Outline each blood parasite and name the species.
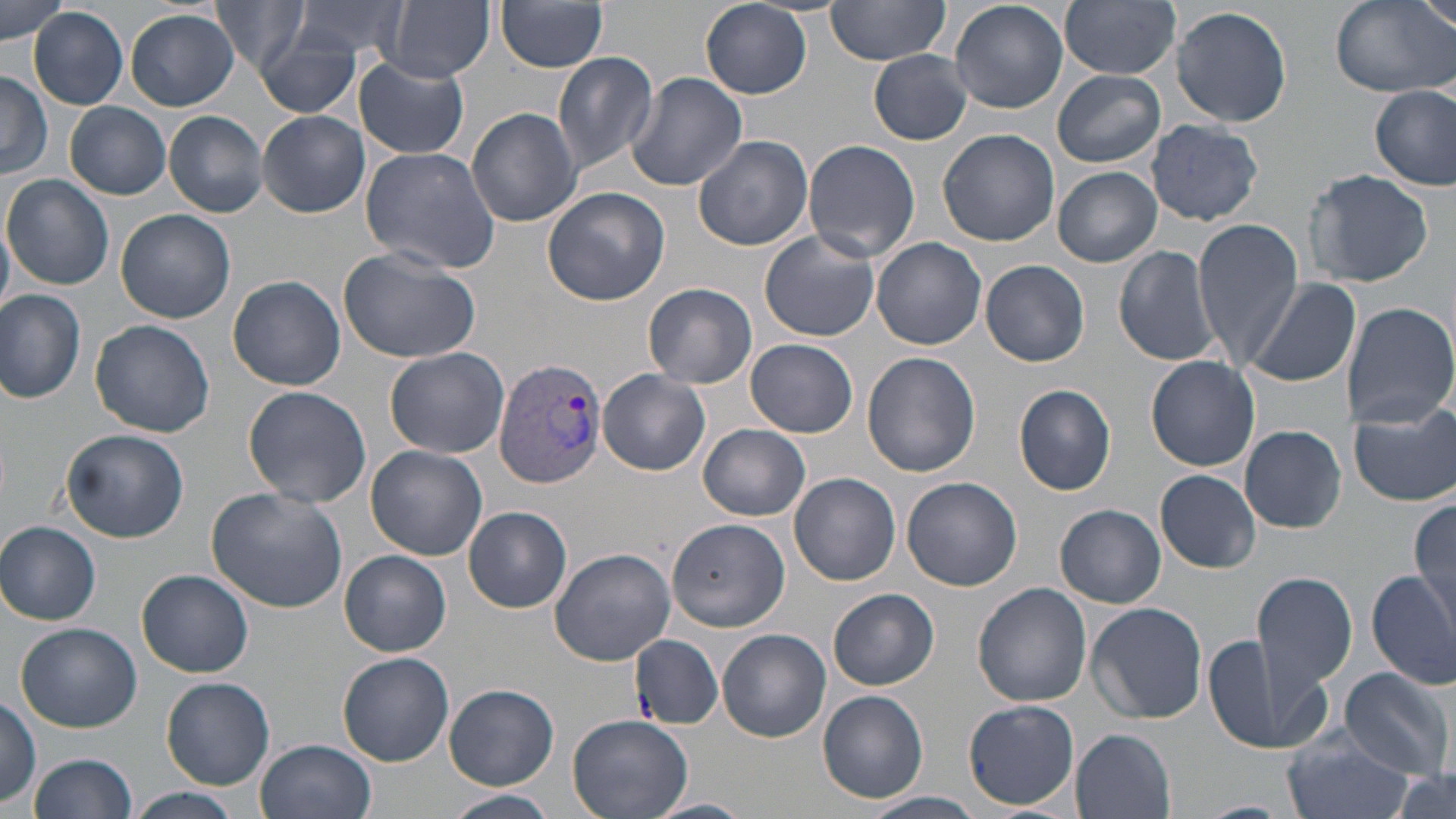
Approximate bounding boxes as (x1,y1)-(x2,y2) corner pairs in pixels.
Plasmodium vivax-infected red blood cells: (495,357)-(611,489).
No Plasmodium falciparum, Plasmodium ovale, Plasmodium malariae, Babesia divergens, or Trypanosoma brucei observed.

Summary:
  - Uninfected red blood cell locations: (0,0)-(70,44), (209,0)-(313,77), (291,0)-(411,62), (384,0)-(494,81), (824,0)-(952,64), (950,0)-(1070,112), (1061,0)-(1181,78), (1330,0)-(1454,98), (1420,0)-(1456,35), (495,1)-(609,72), (700,1)-(812,98), (1170,4)-(1294,129), (28,7)-(129,110), (126,9)-(238,110), (253,31)-(363,117), (870,50)-(974,145), (552,51)-(659,175), (354,55)-(470,160), (0,70)-(50,178), (1052,70)-(1165,167), (624,72)-(748,191), (1371,84)-(1455,191), (65,101)-(172,200), (466,106)-(581,227), (258,110)-(369,218), (164,111)-(269,217), (1147,119)-(1264,226), (938,129)-(1059,246), (693,134)-(814,251), (805,138)-(919,263), (359,146)-(503,275), (1052,165)-(1161,268), (1303,169)-(1433,287), (3,174)-(114,290), (542,186)-(671,306), (116,208)-(236,323), (1194,218)-(1303,370), (0,221)-(14,318), (759,230)-(880,342), (872,238)-(988,351), (1112,245)-(1222,367), (338,246)-(479,364), (980,258)-(1090,367), (227,276)-(346,390), (1246,278)-(1359,390), (643,282)-(757,389), (0,289)-(87,405), (1340,300)-(1456,429), (89,319)-(216,438), (746,339)-(858,438), (384,348)-(509,457), (862,352)-(980,477), (1145,356)-(1260,471), (599,370)-(710,476), (1013,383)-(1116,496), (242,385)-(371,508), (1349,400)-(1456,508), (698,423)-(811,522), (1240,426)-(1348,533), (61,428)-(188,543), (366,446)-(490,562), (1157,471)-(1261,574), (789,473)-(900,584), (901,475)-(1022,591), (206,485)-(351,613), (1412,498)-(1454,634), (1056,505)-(1166,608), (462,506)-(572,614), (667,518)-(790,632), (0,521)-(101,625), (549,545)-(678,666), (341,550)-(451,656), (136,569)-(254,678), (1367,569)-(1456,688), (1251,570)-(1358,702), (971,582)-(1091,705), (828,588)-(938,690), (1086,602)-(1207,723), (15,622)-(141,732), (1203,628)-(1316,752), (718,629)-(831,743), (628,633)-(722,727), (338,651)-(454,766), (1336,666)-(1456,779), (160,676)-(275,788), (444,685)-(559,789), (818,689)-(929,804), (0,696)-(41,807), (963,699)-(1079,810), (566,712)-(692,819), (1072,728)-(1177,818), (1279,728)-(1412,819), (256,737)-(378,819), (27,752)-(136,819), (1388,770)-(1456,819), (125,788)-(244,819), (446,790)-(558,818), (858,791)-(988,819), (643,797)-(754,818)
  - Slide-level diagnosis: Plasmodium vivax
  - Field of view: single
  - Image size: 1456×819 pixels
  - Modality: optical microscopy
  - Stain: May-Grünwald-Giemsa
  - Magnification: 1000x
  - Preparation: thin blood film